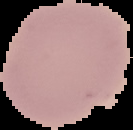

Malaria status: uninfected. From a thin blood film. Image is 133×130 pixels. Cell region segmented out of the field of view; the surrounding area is masked to black.